Assess this cell for malaria.
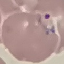
Parasitized.

Summary:
  - Capture: smartphone through the microscope eyepiece
  - Image type: cell patch, automatically extracted from a larger field of view and resized to 64 × 64 pixels
  - Stain: Giemsa
  - Preparation: thin blood film